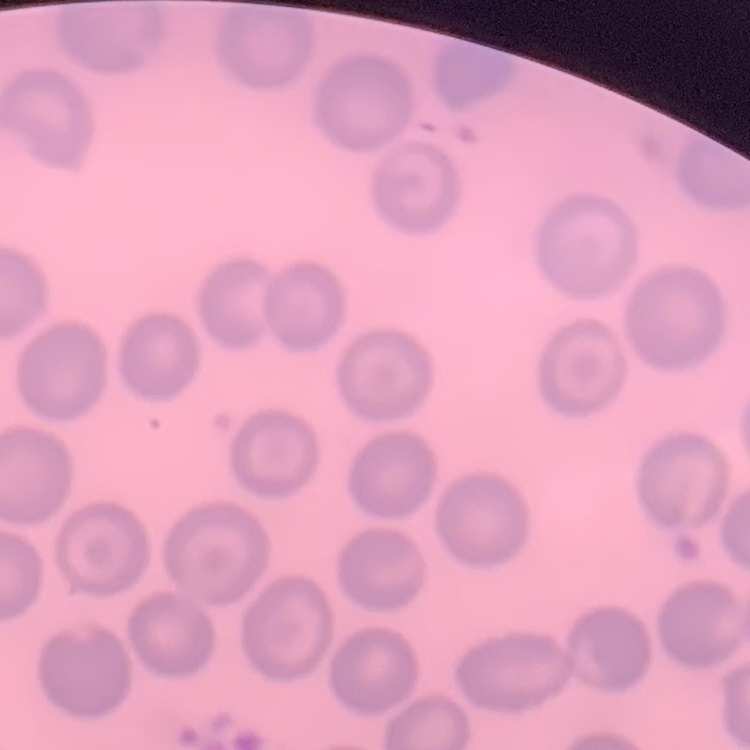
{
  "red_blood_cell_morphology": "no rouleaux formation",
  "stain": "Field's or Giemsa",
  "preparation": "thin blood smear",
  "image_type": "square crop of a larger photomicrograph"
}